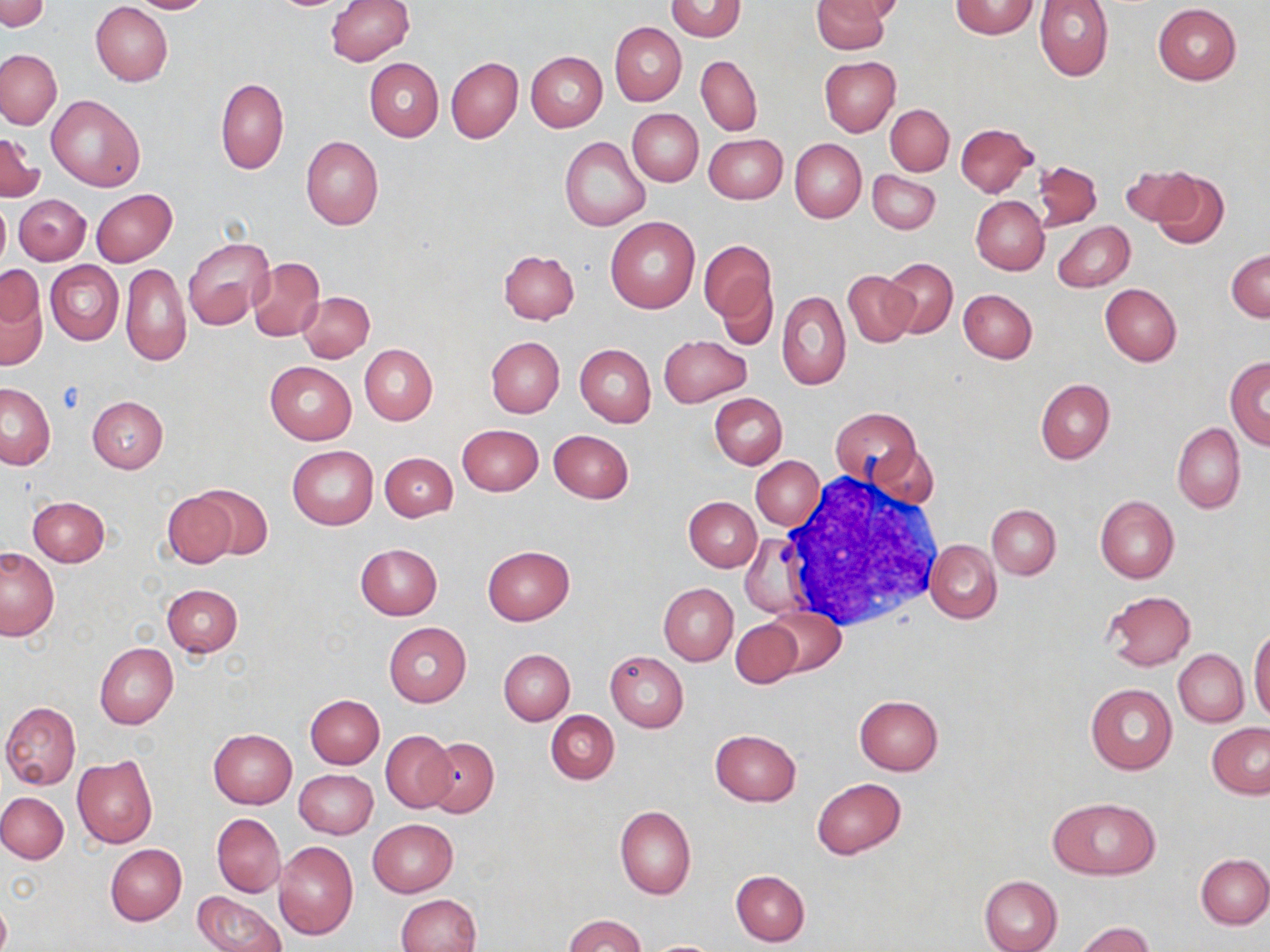
Summary:
  - Coordinate format: approximate bounding boxes as named x1/y1/x2/y2 corners in pixels
  - Uninfected red blood cell locations: (x1=0, y1=0, x2=50, y2=33), (x1=126, y1=0, x2=214, y2=14), (x1=326, y1=0, x2=414, y2=65), (x1=666, y1=0, x2=746, y2=40), (x1=812, y1=0, x2=891, y2=53), (x1=826, y1=0, x2=901, y2=22), (x1=948, y1=0, x2=1040, y2=39), (x1=1034, y1=0, x2=1114, y2=81), (x1=91, y1=2, x2=173, y2=86), (x1=1153, y1=3, x2=1241, y2=84), (x1=609, y1=22, x2=685, y2=105), (x1=0, y1=49, x2=62, y2=129), (x1=526, y1=51, x2=606, y2=131), (x1=697, y1=55, x2=763, y2=135), (x1=446, y1=56, x2=523, y2=143), (x1=820, y1=56, x2=899, y2=137), (x1=364, y1=58, x2=443, y2=141), (x1=216, y1=78, x2=288, y2=175), (x1=46, y1=94, x2=145, y2=191), (x1=886, y1=104, x2=953, y2=174), (x1=628, y1=109, x2=703, y2=186), (x1=955, y1=122, x2=1036, y2=196), (x1=0, y1=134, x2=42, y2=201), (x1=704, y1=134, x2=788, y2=204), (x1=301, y1=136, x2=384, y2=230), (x1=561, y1=137, x2=651, y2=231), (x1=791, y1=139, x2=866, y2=222), (x1=1032, y1=160, x2=1102, y2=229), (x1=1121, y1=164, x2=1199, y2=226), (x1=868, y1=170, x2=940, y2=234), (x1=1150, y1=170, x2=1231, y2=248), (x1=91, y1=188, x2=177, y2=266), (x1=15, y1=193, x2=90, y2=265), (x1=971, y1=195, x2=1049, y2=274), (x1=0, y1=197, x2=10, y2=276), (x1=606, y1=217, x2=700, y2=314), (x1=1053, y1=221, x2=1135, y2=292), (x1=182, y1=238, x2=273, y2=328), (x1=701, y1=243, x2=776, y2=333), (x1=1226, y1=248, x2=1270, y2=321), (x1=498, y1=249, x2=579, y2=325), (x1=248, y1=257, x2=325, y2=341), (x1=882, y1=257, x2=957, y2=338), (x1=46, y1=261, x2=123, y2=345), (x1=120, y1=263, x2=190, y2=366), (x1=843, y1=271, x2=918, y2=347), (x1=0, y1=273, x2=48, y2=370), (x1=715, y1=276, x2=779, y2=351), (x1=1100, y1=283, x2=1181, y2=366), (x1=958, y1=289, x2=1037, y2=363), (x1=299, y1=291, x2=374, y2=362), (x1=778, y1=291, x2=851, y2=390), (x1=660, y1=336, x2=750, y2=405), (x1=486, y1=337, x2=565, y2=417), (x1=359, y1=344, x2=438, y2=424), (x1=575, y1=344, x2=655, y2=428), (x1=1225, y1=356, x2=1270, y2=449), (x1=265, y1=361, x2=356, y2=444), (x1=1035, y1=378, x2=1115, y2=465), (x1=0, y1=383, x2=55, y2=468), (x1=711, y1=392, x2=787, y2=469), (x1=87, y1=396, x2=168, y2=473), (x1=832, y1=407, x2=920, y2=483), (x1=457, y1=423, x2=543, y2=496), (x1=1173, y1=423, x2=1246, y2=513), (x1=548, y1=429, x2=633, y2=503), (x1=869, y1=442, x2=940, y2=509), (x1=287, y1=445, x2=379, y2=530), (x1=379, y1=453, x2=457, y2=521), (x1=752, y1=456, x2=825, y2=530), (x1=192, y1=483, x2=273, y2=561), (x1=163, y1=492, x2=238, y2=569), (x1=1095, y1=494, x2=1180, y2=582), (x1=27, y1=495, x2=110, y2=566), (x1=684, y1=496, x2=762, y2=571), (x1=988, y1=504, x2=1060, y2=580), (x1=740, y1=534, x2=810, y2=617), (x1=926, y1=539, x2=1000, y2=623), (x1=355, y1=543, x2=442, y2=619), (x1=483, y1=545, x2=574, y2=625), (x1=0, y1=548, x2=60, y2=639), (x1=162, y1=583, x2=242, y2=657), (x1=658, y1=584, x2=737, y2=665), (x1=1102, y1=591, x2=1195, y2=670), (x1=765, y1=607, x2=846, y2=677), (x1=731, y1=620, x2=801, y2=688), (x1=384, y1=623, x2=472, y2=707), (x1=1249, y1=629, x2=1270, y2=724), (x1=95, y1=643, x2=177, y2=729), (x1=1185, y1=645, x2=1257, y2=792), (x1=499, y1=648, x2=574, y2=725), (x1=1174, y1=649, x2=1249, y2=726), (x1=605, y1=652, x2=687, y2=732), (x1=1085, y1=684, x2=1177, y2=774), (x1=854, y1=694, x2=944, y2=775), (x1=305, y1=695, x2=384, y2=768), (x1=2, y1=702, x2=81, y2=791), (x1=546, y1=711, x2=619, y2=784), (x1=1207, y1=723, x2=1270, y2=798), (x1=208, y1=728, x2=297, y2=808), (x1=709, y1=728, x2=802, y2=806), (x1=381, y1=729, x2=457, y2=811), (x1=424, y1=738, x2=498, y2=818), (x1=72, y1=754, x2=157, y2=848), (x1=295, y1=770, x2=378, y2=839), (x1=812, y1=778, x2=906, y2=859), (x1=0, y1=792, x2=68, y2=864), (x1=1047, y1=796, x2=1160, y2=880), (x1=615, y1=806, x2=696, y2=900), (x1=212, y1=813, x2=285, y2=896), (x1=367, y1=818, x2=457, y2=896), (x1=274, y1=842, x2=359, y2=939), (x1=105, y1=844, x2=186, y2=925), (x1=1196, y1=855, x2=1270, y2=928), (x1=731, y1=870, x2=810, y2=946), (x1=979, y1=874, x2=1063, y2=952), (x1=194, y1=890, x2=286, y2=952), (x1=397, y1=894, x2=482, y2=952), (x1=0, y1=895, x2=11, y2=952), (x1=565, y1=915, x2=644, y2=952), (x1=1073, y1=922, x2=1156, y2=952), (x1=648, y1=940, x2=720, y2=951)
  - White blood cell locations: (x1=775, y1=477, x2=945, y2=630)
  - Slide-level diagnosis: negative for blood parasites
  - Preparation: thin blood film
  - Modality: light microscopy
  - Magnification: 1000x
  - Stain: May-Grünwald-Giemsa
  - Image size: 1270×952 pixels
  - Field of view: one of a larger specimen